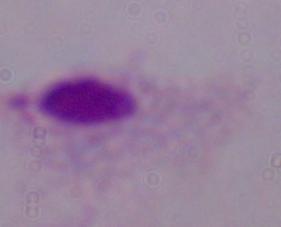
Summary:
  - Modality: photomicrograph
  - Magnification: 1000x
  - Identification: trichomonad